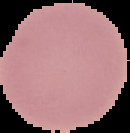 Image is 130×133 pixels. Cell region segmented out of the field of view; the surrounding area is masked to black. Malaria status: uninfected. From a thin blood film.